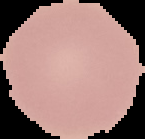
Summary:
  - Image size: 145×139 pixels
  - Preparation: thin blood film
  - Result: negative for Plasmodium parasites
  - Image type: cell region segmented out of the field of view; surrounding area masked to black